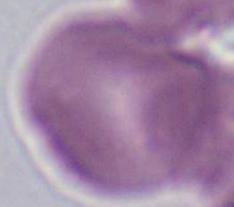

Micrograph. A red blood cell is seen. 1000x magnification.